Name the parasite shown.
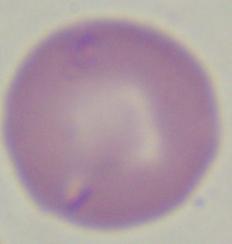

This is Babesia.

1000x magnification. Micrograph.